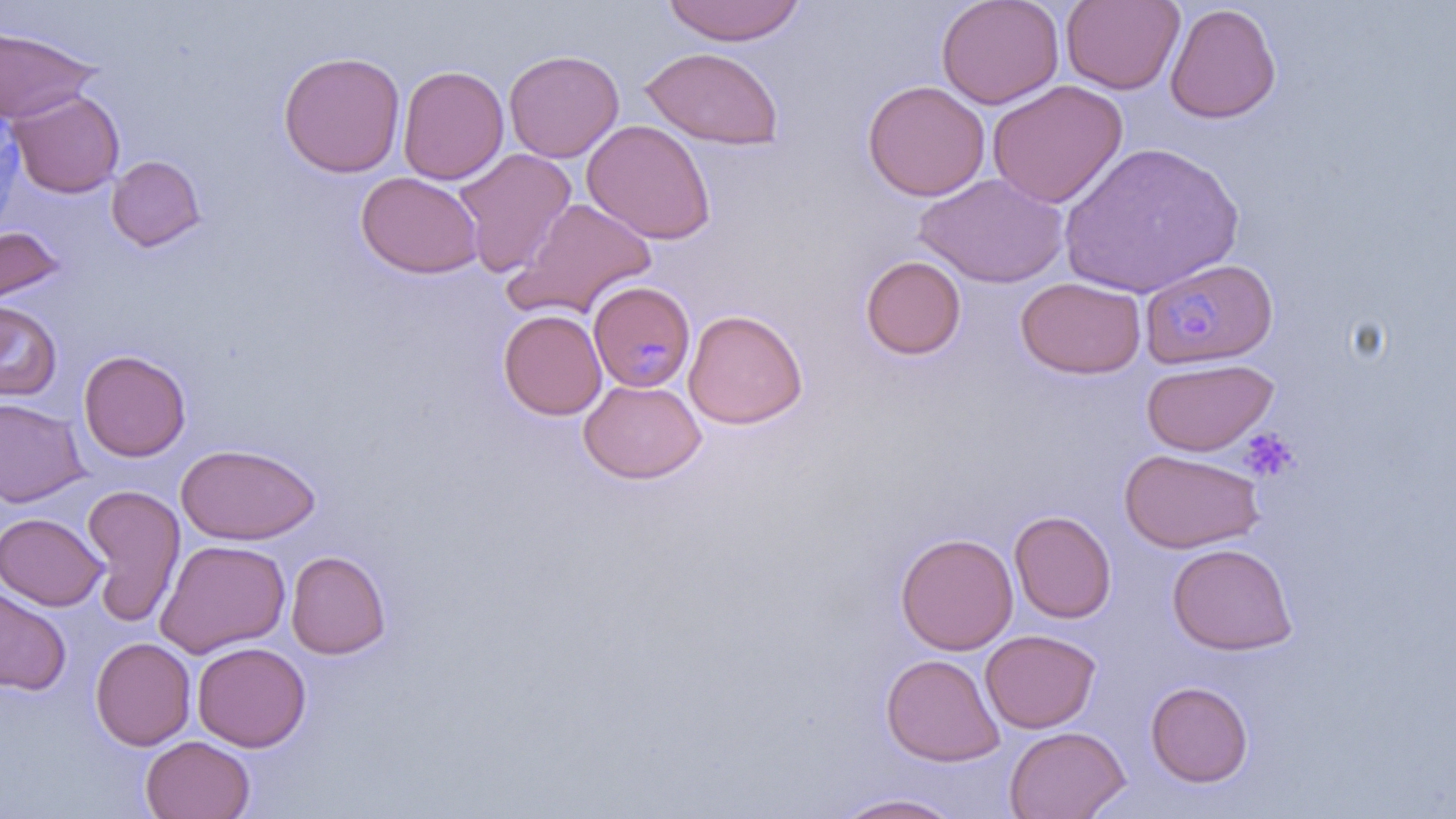

Approximate bounding boxes as (x1, y1, x2, y2) in pixels. Plasmodium malariae-infected red blood cell locations: (1139, 257, 1278, 369), (588, 281, 696, 392). Uninfected red blood cell locations: (937, 0, 1063, 109), (1060, 0, 1184, 94), (662, 1, 806, 45), (1165, 3, 1282, 124), (0, 26, 100, 125), (641, 46, 785, 150), (503, 49, 624, 163), (279, 51, 405, 177), (397, 64, 509, 184), (862, 79, 990, 201), (987, 80, 1128, 208), (9, 90, 125, 198), (581, 119, 717, 245), (1055, 140, 1247, 299), (453, 147, 577, 278), (106, 155, 206, 251), (355, 172, 484, 279), (914, 172, 1069, 288), (509, 196, 657, 320), (0, 225, 66, 310), (860, 255, 966, 359), (1015, 277, 1146, 379), (0, 299, 62, 401), (684, 308, 808, 430), (498, 310, 607, 420), (78, 349, 191, 462), (1141, 357, 1279, 456), (578, 379, 707, 484), (0, 398, 89, 508), (175, 444, 321, 544), (1120, 448, 1264, 553), (81, 484, 186, 625), (1009, 510, 1116, 623), (0, 512, 108, 610), (895, 532, 1018, 655), (154, 539, 291, 658), (1166, 542, 1298, 655), (286, 550, 391, 659), (0, 587, 72, 695), (980, 628, 1101, 733), (90, 636, 196, 750), (192, 641, 311, 752), (881, 653, 1005, 766), (1145, 680, 1254, 787), (1004, 725, 1130, 819), (140, 735, 255, 819), (831, 792, 967, 818). Platelet locations: (1237, 426, 1299, 483). Slide-level diagnosis: Plasmodium malariae. One field of a larger specimen. May-Grünwald-Giemsa stain. Captured at 1000x magnification. Image is 1456×819 pixels. Light microscopy. Thin blood smear.